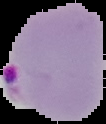 Malaria status: parasitized. Image is 106×124 pixels. Cell region segmented out of the field of view; the surrounding area is masked to black. From a thin blood smear.